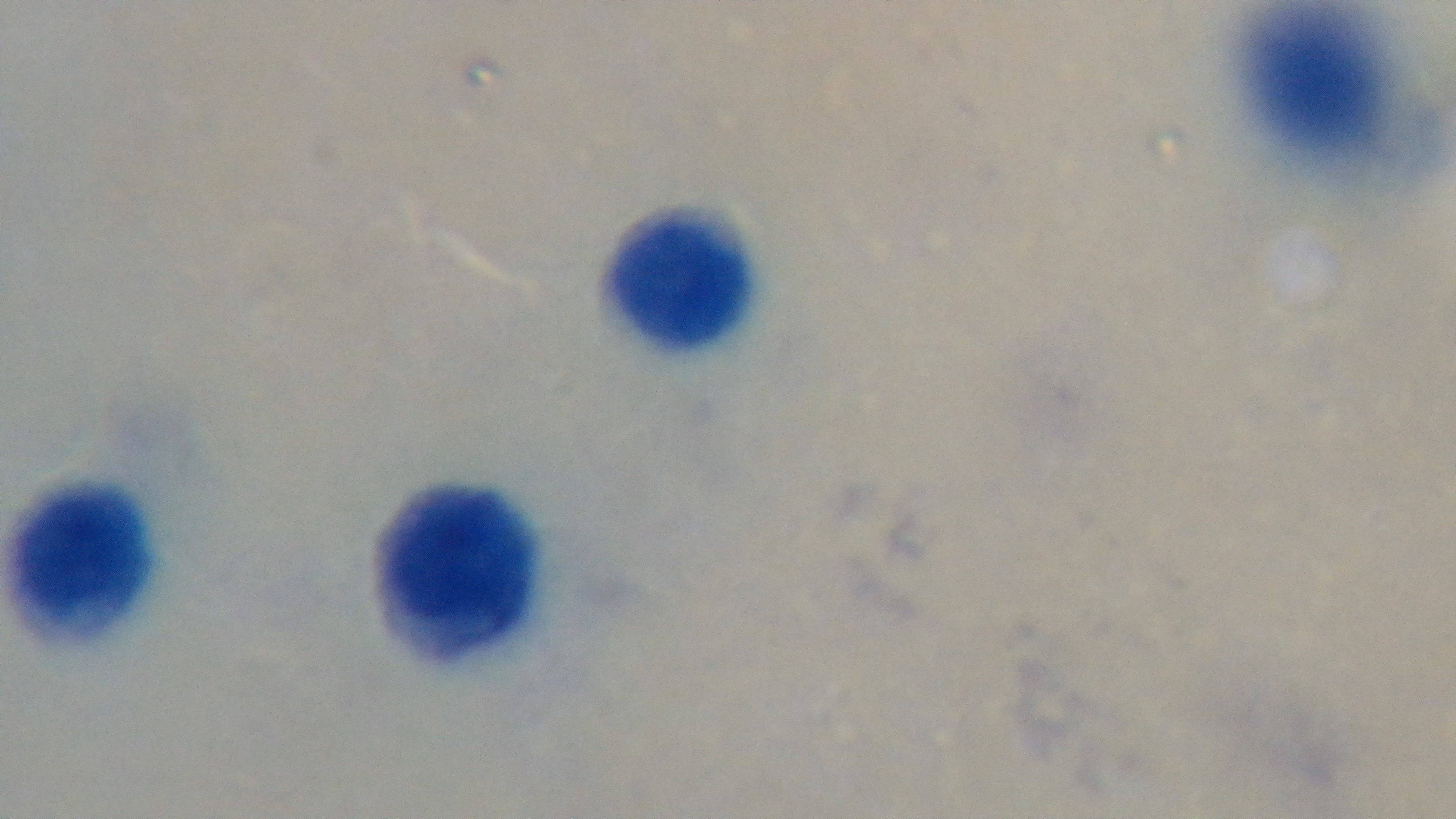
Summary:
  - Capture: mounted 4K digital camera
  - Modality: light microscopy
  - Preparation: thick blood film
  - Field of view: single
  - Malaria status: negative
  - Stain: Giemsa
  - Objective: 100x oil immersion